Describe the morphology of the red blood cells.
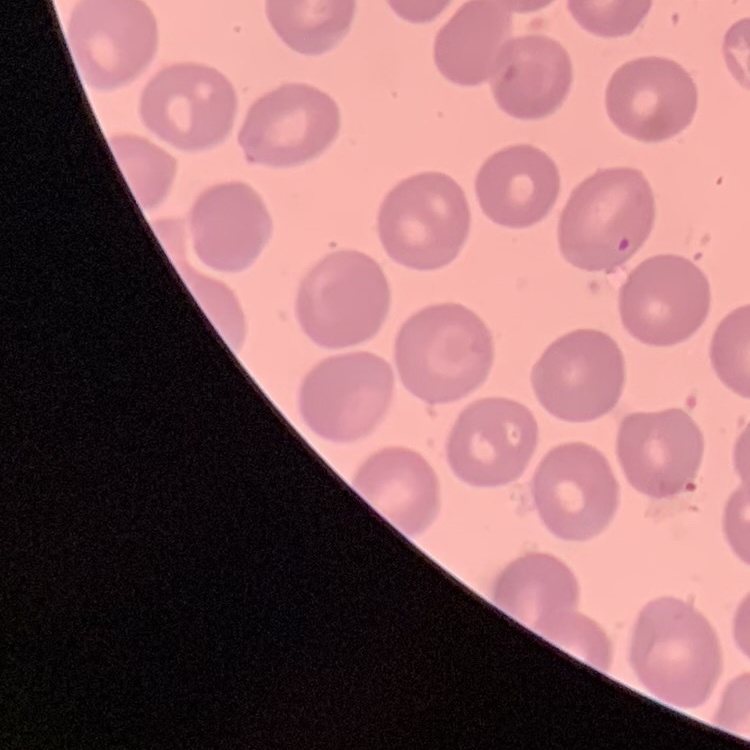

They show no rouleaux formation.

Stained with either Field's or Giemsa. Thin blood smear. One tile cut from a larger photomicrograph.